Report the malaria status of this cell.
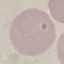
It is uninfected.

Summary:
  - Stain: Giemsa
  - Preparation: thin blood smear
  - Capture: smartphone camera at the microscope eyepiece
  - Image type: automatically extracted cell patch, resized to 64 × 64 pixels